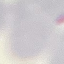

result = negative for malaria parasites
preparation = thin blood film
image type = automatically extracted cell patch, resized to 64 × 64 pixels
capture = smartphone through the microscope eyepiece
stain = Giemsa